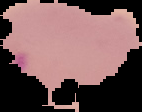
Image is 142×112 pixels. Segmented cell region on a black background. From a thin blood smear. Malaria status: uninfected.